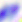

identification = Toxoplasma gondii
magnification = 400x
modality = photomicrograph